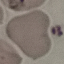
Summary:
  - Malaria status: uninfected
  - Preparation: thin smear
  - Capture: smartphone camera at the microscope eyepiece
  - Image type: automatically extracted cell patch, resized to 64 × 64 pixels
  - Stain: Giemsa